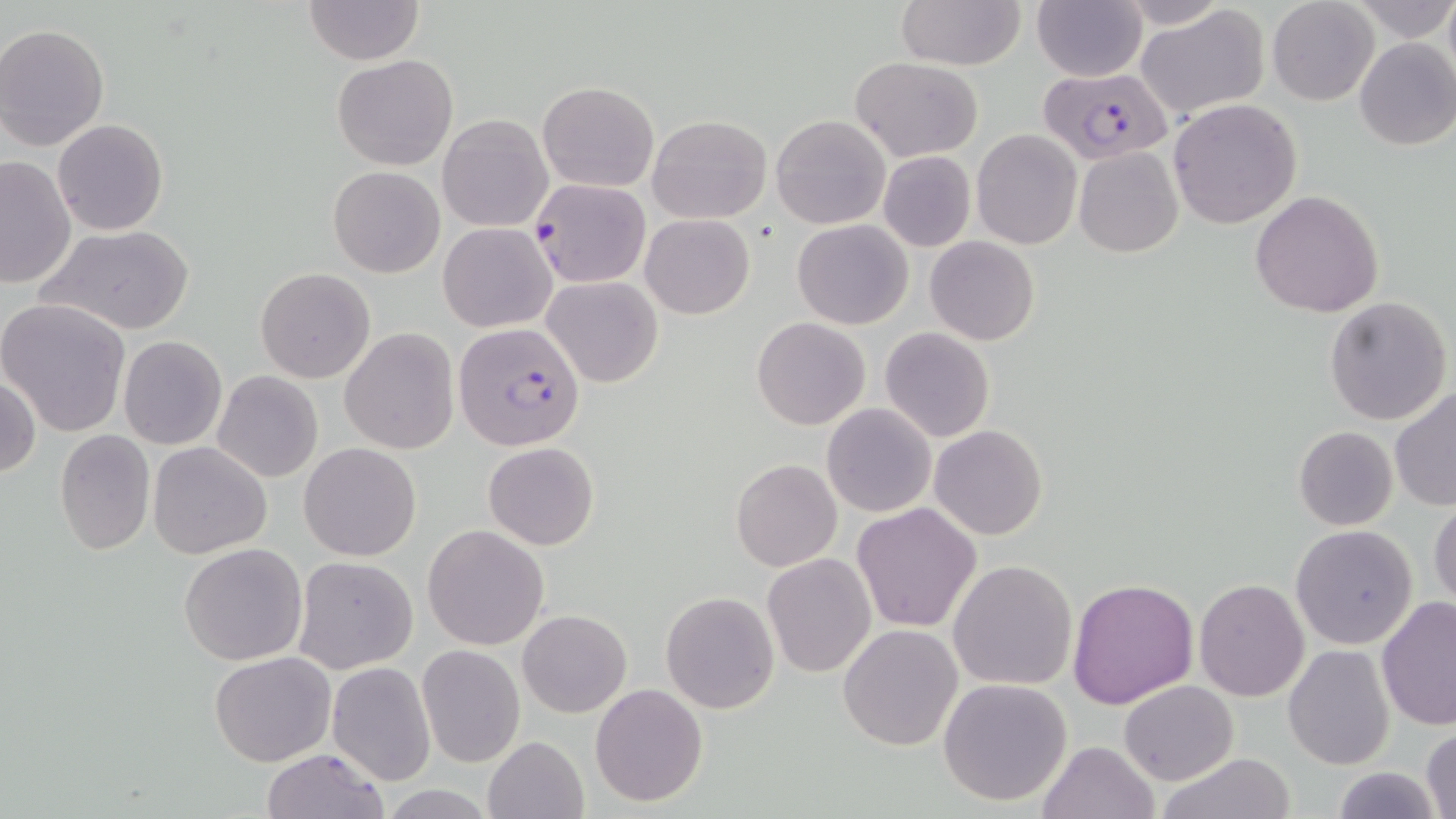
Approximate bounding boxes as [x1, y1, x2, y2] in pixels. Plasmodium falciparum-infected red blood cell locations (subset): [1036, 67, 1174, 164], [531, 177, 650, 288]. Uninfected red blood cell locations (subset): [301, 0, 424, 66], [895, 0, 1025, 70], [1031, 0, 1147, 82], [1114, 0, 1231, 29], [1267, 0, 1379, 106], [1347, 1, 1453, 40], [1137, 5, 1272, 122], [1, 23, 114, 152], [1353, 37, 1456, 150], [332, 55, 458, 171], [852, 56, 982, 161], [538, 81, 658, 192], [1168, 99, 1300, 229], [771, 113, 890, 229], [437, 114, 552, 232], [647, 114, 771, 224], [52, 118, 168, 236], [972, 130, 1082, 249], [1074, 147, 1183, 259], [878, 150, 977, 252], [0, 154, 76, 290], [328, 166, 444, 278], [1250, 190, 1384, 316], [641, 214, 754, 319], [792, 219, 912, 330], [439, 223, 557, 332], [39, 224, 194, 336], [925, 236, 1040, 347], [255, 267, 375, 383], [542, 275, 662, 388], [1324, 296, 1452, 426], [0, 299, 133, 437], [752, 317, 870, 430], [880, 327, 995, 442], [339, 328, 460, 455], [118, 335, 228, 450], [211, 371, 323, 482], [0, 372, 40, 480], [1390, 385, 1456, 511], [822, 403, 936, 517], [930, 425, 1048, 541], [1293, 426, 1398, 531], [53, 430, 155, 554], [148, 442, 273, 560], [298, 442, 422, 561], [484, 442, 599, 549], [731, 459, 841, 572], [1429, 496, 1456, 610], [851, 503, 981, 633], [423, 524, 549, 649], [1290, 525, 1418, 649], [178, 542, 309, 666], [761, 553, 878, 678], [292, 556, 418, 673], [948, 558, 1078, 690], [1067, 576, 1199, 709], [1194, 578, 1309, 702], [660, 591, 780, 712], [1376, 594, 1456, 733], [517, 608, 632, 718], [838, 624, 964, 750], [416, 643, 525, 767], [1283, 645, 1394, 769], [210, 650, 335, 765], [327, 662, 437, 785], [938, 678, 1073, 806], [1119, 680, 1237, 785], [590, 683, 709, 806], [1420, 728, 1455, 819], [483, 735, 589, 819], [1036, 740, 1161, 819], [259, 747, 390, 819], [1157, 752, 1295, 819], [1331, 766, 1442, 819]. Slide-level diagnosis: Plasmodium falciparum. Light microscopy. Captured at 1000x magnification. Single field of view. Image is 1456×819 pixels. May-Grünwald-Giemsa stain. Thin blood film.